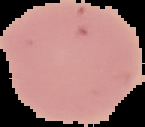
preparation = thin blood smear
image size = 145×127 pixels
malaria status = uninfected
image type = segmented cell region on a black background